Locate and identify every blood parasite.
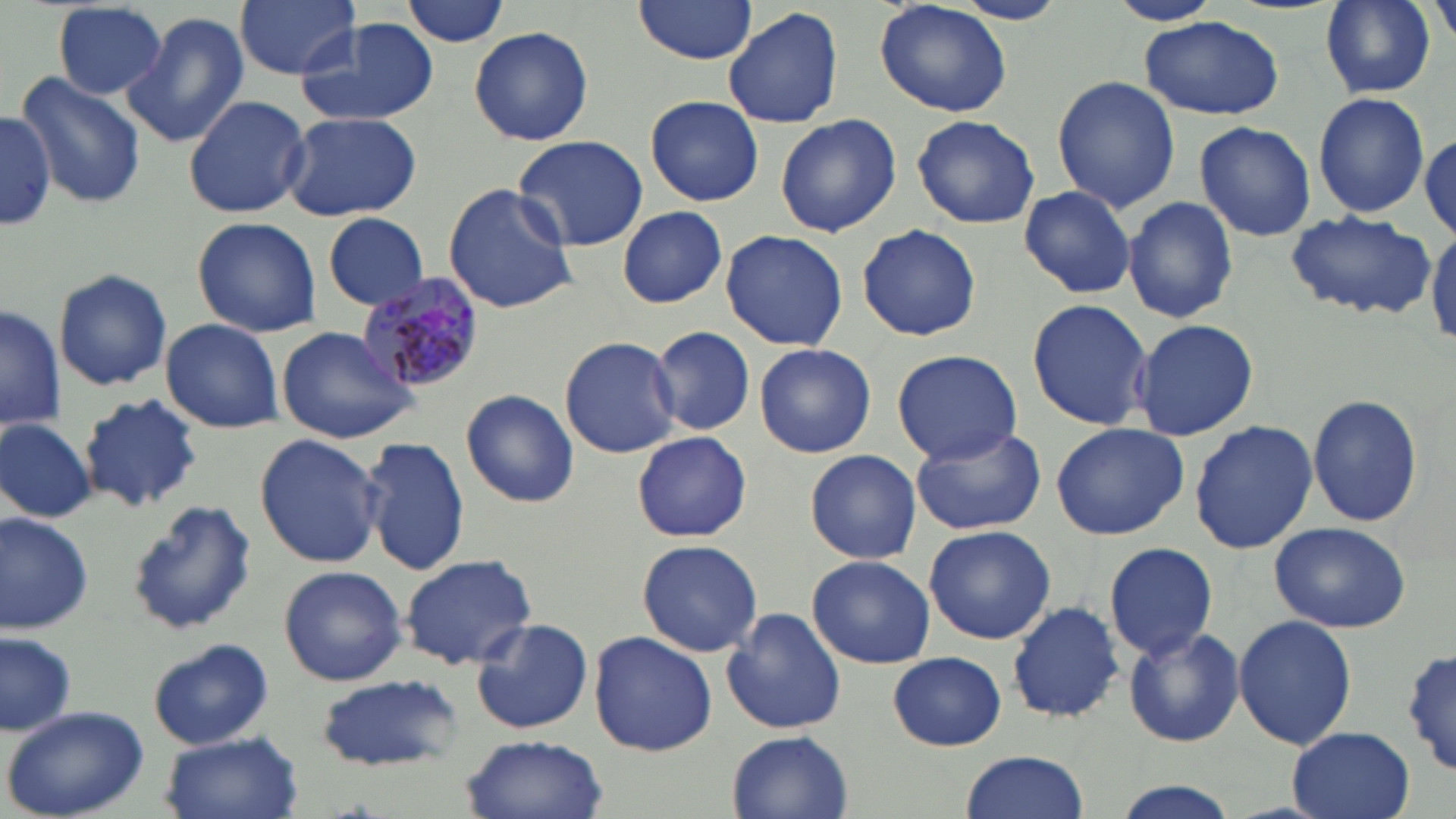
Approximate bounding boxes as [x1, y1, x2, y2] in pixels.
Plasmodium malariae-infected red blood cells: [359, 275, 488, 397].
No Plasmodium falciparum, Plasmodium ovale, Plasmodium vivax, Babesia divergens, or Trypanosoma brucei observed.

slide_level_diagnosis: Plasmodium malariae
modality: light microscopy
magnification: 1000x
stain: May-Grünwald-Giemsa
image_size: 1456×819 pixels
field_of_view: single
uninfected_red_blood_cell_locations: 'approximate bounding boxes as [x1, y1, x2, y2] in pixels: [234, 0, 360, 79], [399, 0, 512, 47], [632, 0, 758, 65], [876, 0, 1013, 119], [1107, 0, 1222, 26], [948, 1, 1074, 25], [1319, 1, 1434, 98], [51, 2, 169, 98], [723, 5, 844, 129], [121, 13, 252, 147], [296, 16, 441, 129], [1140, 16, 1283, 120], [469, 25, 594, 148], [15, 71, 146, 210], [1051, 75, 1180, 213], [1314, 92, 1429, 218], [184, 94, 311, 219], [644, 94, 763, 206], [0, 109, 55, 232], [281, 110, 421, 222], [774, 113, 902, 239], [912, 114, 1040, 232], [1194, 120, 1317, 242], [1419, 129, 1455, 241], [511, 134, 650, 252], [442, 183, 579, 315], [1017, 185, 1140, 299], [1123, 196, 1239, 324], [617, 206, 728, 308], [1284, 212, 1436, 320], [322, 213, 430, 309], [192, 216, 322, 338], [856, 224, 982, 342], [1428, 226, 1456, 348], [720, 229, 848, 352], [53, 269, 173, 391], [1026, 297, 1153, 430], [2, 302, 66, 430], [1132, 316, 1258, 443], [160, 319, 284, 434], [650, 325, 755, 436], [276, 326, 419, 444], [559, 336, 682, 459], [754, 342, 876, 458], [889, 350, 1023, 464], [459, 388, 579, 508], [1307, 392, 1425, 529], [77, 394, 203, 514], [1, 418, 96, 521], [1190, 420, 1319, 553], [1048, 421, 1190, 540], [907, 423, 1048, 537], [630, 430, 754, 543], [255, 432, 382, 569], [361, 436, 470, 577], [805, 449, 921, 564], [128, 498, 257, 636], [0, 510, 95, 634], [1267, 519, 1412, 634], [924, 525, 1056, 645], [636, 539, 764, 659], [1103, 542, 1218, 661], [399, 553, 536, 671], [808, 554, 936, 669], [277, 566, 407, 685], [1007, 601, 1127, 722], [722, 608, 845, 736], [1234, 613, 1357, 752], [471, 616, 593, 734], [1123, 627, 1246, 749], [0, 630, 76, 737], [588, 630, 717, 756], [148, 639, 274, 751], [1402, 646, 1454, 779], [888, 652, 1007, 750], [315, 674, 460, 771], [2, 705, 151, 818], [1285, 728, 1415, 819], [728, 730, 853, 819], [159, 731, 303, 819], [462, 733, 608, 819], [958, 751, 1090, 819], [1108, 779, 1245, 819]'
preparation: thin blood film